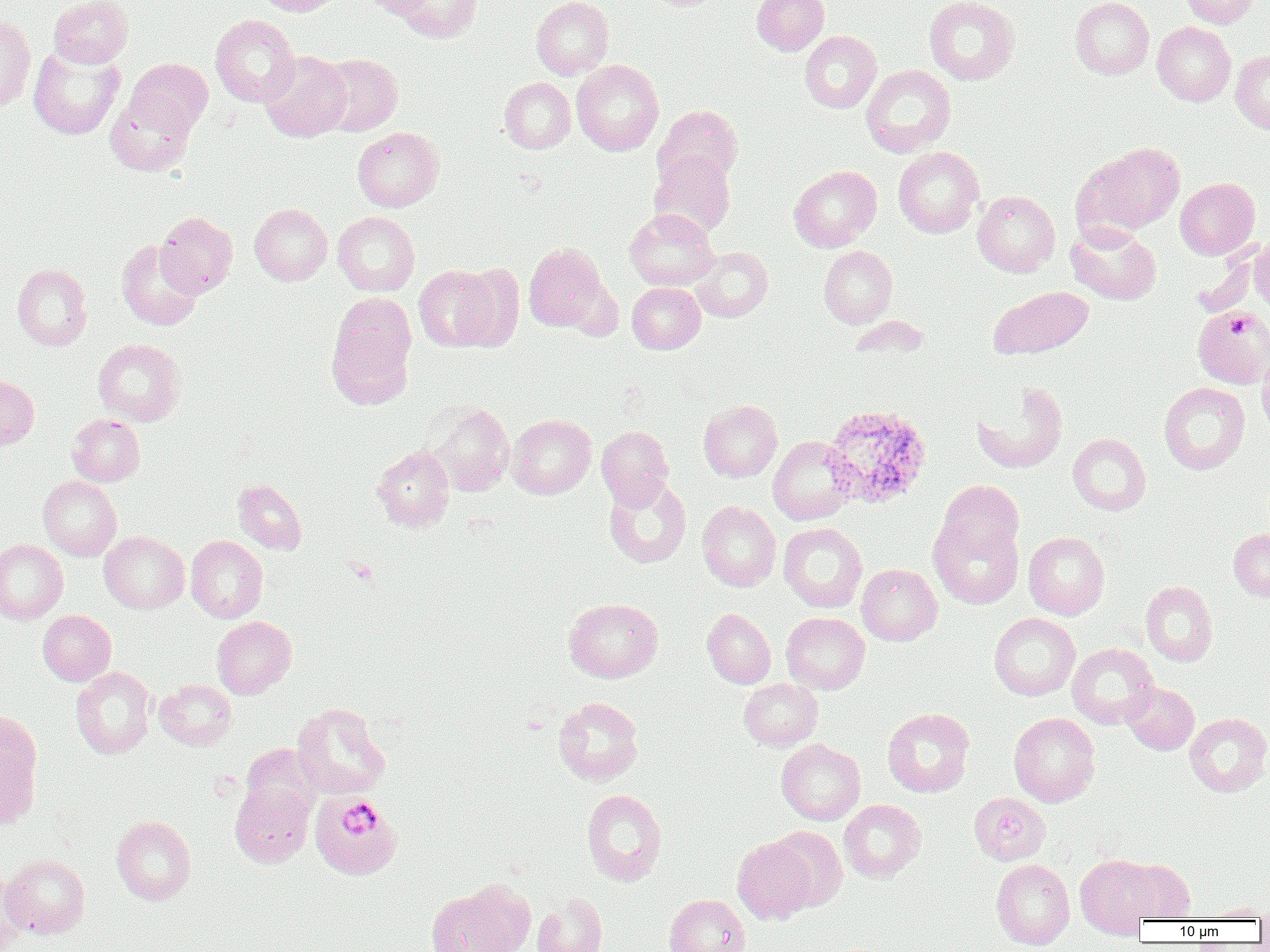
Approximate bounding boxes as [x1, y1, x2, y2] in pixels. Platelet locations: [1229, 310, 1251, 338], [346, 557, 378, 585], [340, 804, 379, 838]. Plasmodium ovale-infected red blood cell locations: [822, 404, 932, 509]. Uninfected red blood cell locations: [48, 0, 133, 67], [254, 0, 344, 16], [362, 0, 433, 18], [390, 0, 483, 43], [531, 0, 613, 79], [751, 0, 829, 55], [924, 0, 1019, 85], [1070, 0, 1154, 79], [1179, 0, 1259, 27], [0, 13, 35, 112], [210, 14, 300, 106], [1152, 22, 1236, 106], [800, 31, 881, 113], [28, 45, 124, 139], [260, 51, 351, 141], [1231, 51, 1270, 133], [317, 53, 402, 136], [126, 58, 213, 136], [572, 60, 664, 156], [861, 65, 956, 157], [499, 77, 576, 153], [105, 92, 196, 176], [654, 104, 743, 187], [352, 127, 443, 211], [1087, 142, 1186, 234], [893, 147, 984, 238], [649, 150, 736, 238], [788, 165, 882, 252], [1175, 177, 1260, 259], [973, 190, 1060, 277], [249, 203, 332, 285], [625, 208, 719, 290], [155, 212, 238, 297], [333, 212, 419, 296], [1066, 224, 1162, 305], [1249, 239, 1270, 316], [116, 240, 203, 331], [1222, 241, 1270, 318], [523, 242, 610, 332], [691, 246, 772, 322], [818, 246, 897, 327], [453, 262, 524, 352], [12, 264, 92, 350], [413, 264, 501, 351], [627, 282, 705, 353], [991, 286, 1093, 358], [1192, 306, 1270, 389], [327, 315, 415, 409], [848, 315, 929, 361], [93, 338, 185, 425], [1257, 347, 1270, 440], [0, 375, 39, 449], [972, 382, 1068, 473], [1159, 382, 1250, 474], [698, 400, 782, 482], [427, 403, 514, 496], [67, 414, 145, 486], [507, 414, 596, 498], [597, 425, 673, 509], [1067, 434, 1151, 515], [768, 436, 857, 525], [372, 446, 455, 531], [38, 476, 121, 560], [604, 477, 692, 569], [233, 478, 307, 554], [937, 480, 1024, 564], [697, 501, 781, 592], [929, 516, 1023, 609], [779, 522, 867, 612], [1228, 527, 1270, 601], [99, 532, 189, 613], [1024, 532, 1110, 620], [186, 535, 267, 623], [0, 539, 68, 624], [856, 564, 942, 645], [1141, 581, 1218, 666], [564, 598, 664, 682], [702, 608, 775, 689], [37, 610, 116, 686], [781, 612, 870, 694], [989, 612, 1080, 700], [212, 616, 297, 698], [1067, 643, 1159, 729], [71, 667, 155, 759], [739, 678, 822, 750], [154, 679, 236, 750], [1122, 682, 1199, 755], [553, 697, 643, 785], [292, 703, 390, 799], [882, 708, 975, 797], [1009, 713, 1100, 806], [1185, 713, 1270, 796], [0, 728, 41, 829], [776, 738, 865, 825], [241, 744, 322, 821], [230, 782, 314, 867], [581, 789, 666, 886], [969, 792, 1050, 865], [318, 797, 407, 881], [839, 800, 926, 882], [111, 816, 197, 905], [768, 826, 848, 911], [732, 837, 817, 925], [1, 854, 90, 938], [1075, 855, 1160, 938], [1120, 858, 1195, 923], [991, 859, 1075, 949], [0, 871, 29, 952], [426, 887, 523, 951], [532, 893, 608, 952], [664, 894, 750, 952], [1204, 903, 1270, 920]. Slide-level diagnosis: Plasmodium ovale. Single field of view. Image is 1270×952 pixels. Thin blood smear. Optical microscopy. 1000x magnification.